Name the parasite shown.
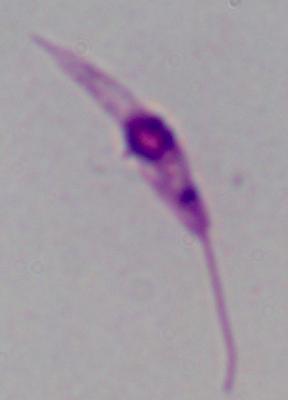

Leishmania.

Captured at 1000x magnification. Photomicrograph.